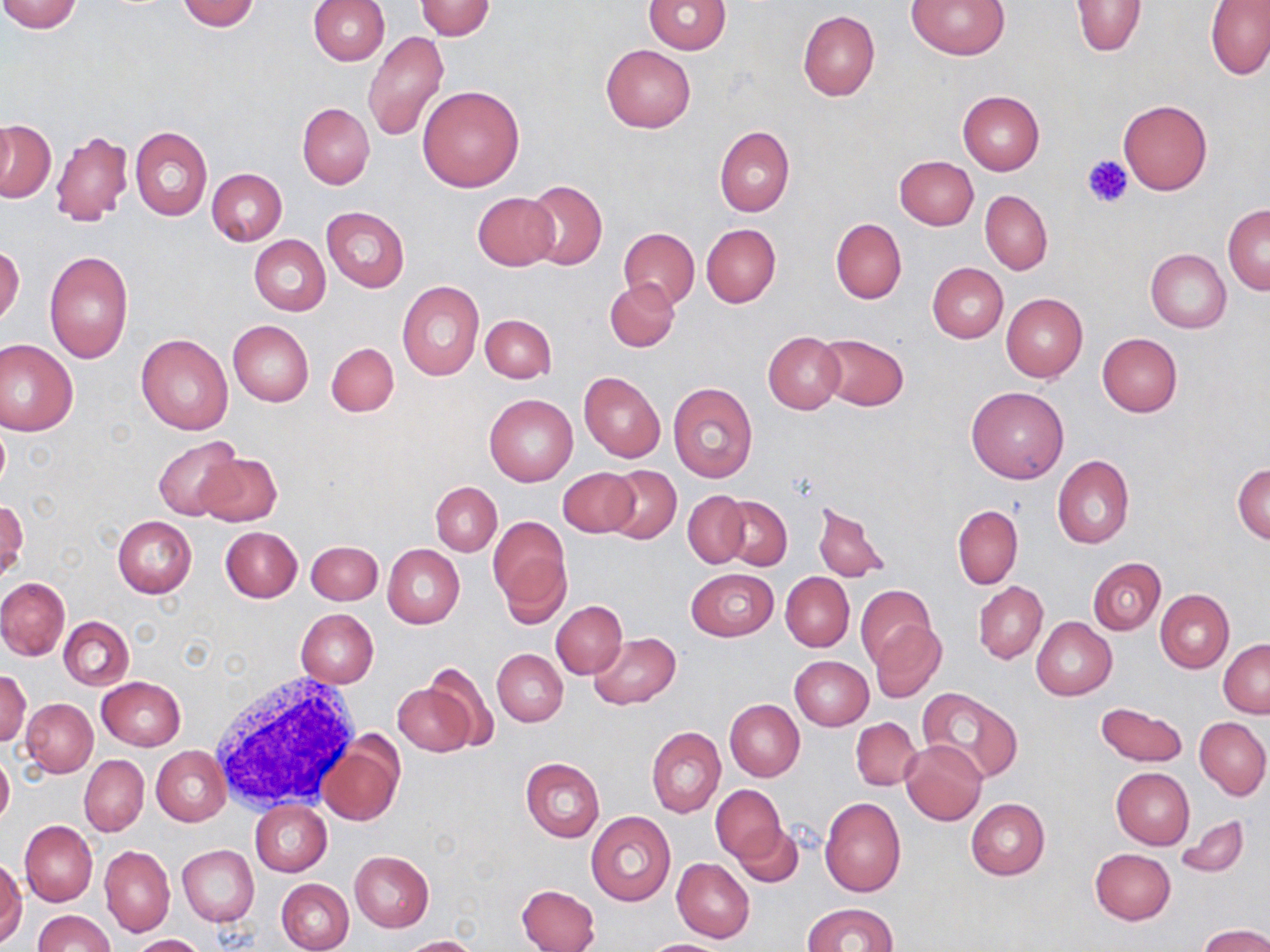

Summary:
  - Coordinate format: approximate bounding boxes as (x1, y1, x2, y2) in pixels
  - White blood cell locations: (207, 671, 365, 813)
  - Uninfected red blood cell locations: (0, 0, 82, 33), (178, 0, 259, 31), (309, 0, 390, 65), (908, 0, 1009, 59), (416, 1, 494, 40), (644, 1, 732, 53), (1072, 2, 1145, 56), (1206, 2, 1270, 80), (797, 11, 879, 101), (361, 31, 449, 143), (601, 45, 695, 132), (417, 85, 525, 192), (957, 90, 1045, 174), (1118, 99, 1212, 195), (298, 103, 375, 189), (1, 121, 55, 202), (715, 125, 795, 216), (130, 126, 212, 220), (50, 131, 133, 226), (894, 155, 979, 229), (207, 168, 287, 246), (522, 180, 607, 271), (980, 191, 1052, 275), (472, 192, 559, 270), (1223, 204, 1270, 294), (321, 207, 409, 292), (830, 217, 906, 303), (701, 224, 781, 307), (618, 227, 700, 309), (249, 235, 330, 316), (0, 246, 25, 325), (1145, 248, 1231, 332), (44, 250, 134, 363), (928, 262, 1008, 343), (604, 278, 678, 352), (397, 280, 484, 380), (1001, 294, 1087, 381), (480, 313, 557, 383), (228, 320, 314, 406), (763, 332, 844, 413), (817, 333, 909, 411), (136, 334, 234, 436), (1097, 334, 1182, 417), (0, 339, 78, 435), (326, 342, 398, 417), (578, 371, 665, 463), (668, 383, 759, 482), (967, 386, 1068, 483), (484, 394, 579, 486), (152, 436, 239, 519), (199, 451, 281, 527), (1052, 455, 1133, 549), (1233, 462, 1270, 544), (602, 466, 681, 543), (559, 468, 640, 539), (430, 481, 501, 556), (683, 491, 750, 569), (721, 497, 793, 569), (1, 500, 27, 584), (813, 501, 890, 584), (952, 504, 1023, 589), (113, 516, 197, 598), (488, 516, 570, 617), (220, 527, 302, 602), (306, 541, 383, 605), (383, 544, 465, 629), (1088, 557, 1166, 634), (686, 568, 777, 642), (781, 572, 854, 652), (0, 577, 70, 660), (973, 581, 1047, 663), (855, 585, 935, 671), (1155, 590, 1234, 672), (551, 601, 627, 678), (297, 609, 379, 688), (60, 617, 133, 690), (1032, 617, 1117, 700), (872, 620, 946, 703), (589, 633, 680, 708), (1218, 639, 1270, 717), (493, 649, 567, 727), (789, 655, 874, 730), (419, 661, 503, 751), (0, 668, 31, 748), (97, 676, 186, 751), (391, 682, 478, 756), (916, 690, 1022, 784), (21, 699, 98, 777), (725, 700, 805, 781), (1096, 703, 1186, 766), (1195, 716, 1270, 799), (851, 718, 921, 790), (647, 727, 725, 817), (320, 736, 403, 827), (901, 741, 987, 825), (152, 745, 229, 827), (0, 750, 14, 827), (79, 756, 149, 836), (520, 757, 605, 841), (1111, 767, 1194, 849), (710, 784, 785, 863), (820, 796, 906, 896), (965, 798, 1050, 880), (250, 799, 331, 877), (586, 813, 676, 907), (1176, 815, 1248, 879), (20, 820, 97, 906), (734, 823, 805, 888), (100, 845, 175, 938), (177, 845, 258, 926), (1090, 848, 1175, 924), (350, 851, 433, 931), (672, 858, 755, 943), (0, 859, 25, 945), (276, 879, 353, 952), (517, 883, 601, 952), (804, 902, 899, 952), (33, 910, 113, 952), (1199, 924, 1270, 952), (132, 934, 204, 951), (401, 935, 478, 952), (642, 939, 731, 952)
  - Platelet locations: (1082, 155, 1132, 209)
  - Slide-level diagnosis: negative for blood parasites
  - Field of view: single
  - Modality: optical microscopy
  - Stain: May-Grünwald-Giemsa
  - Image size: 1270×952 pixels
  - Preparation: thin blood smear
  - Magnification: 1000x